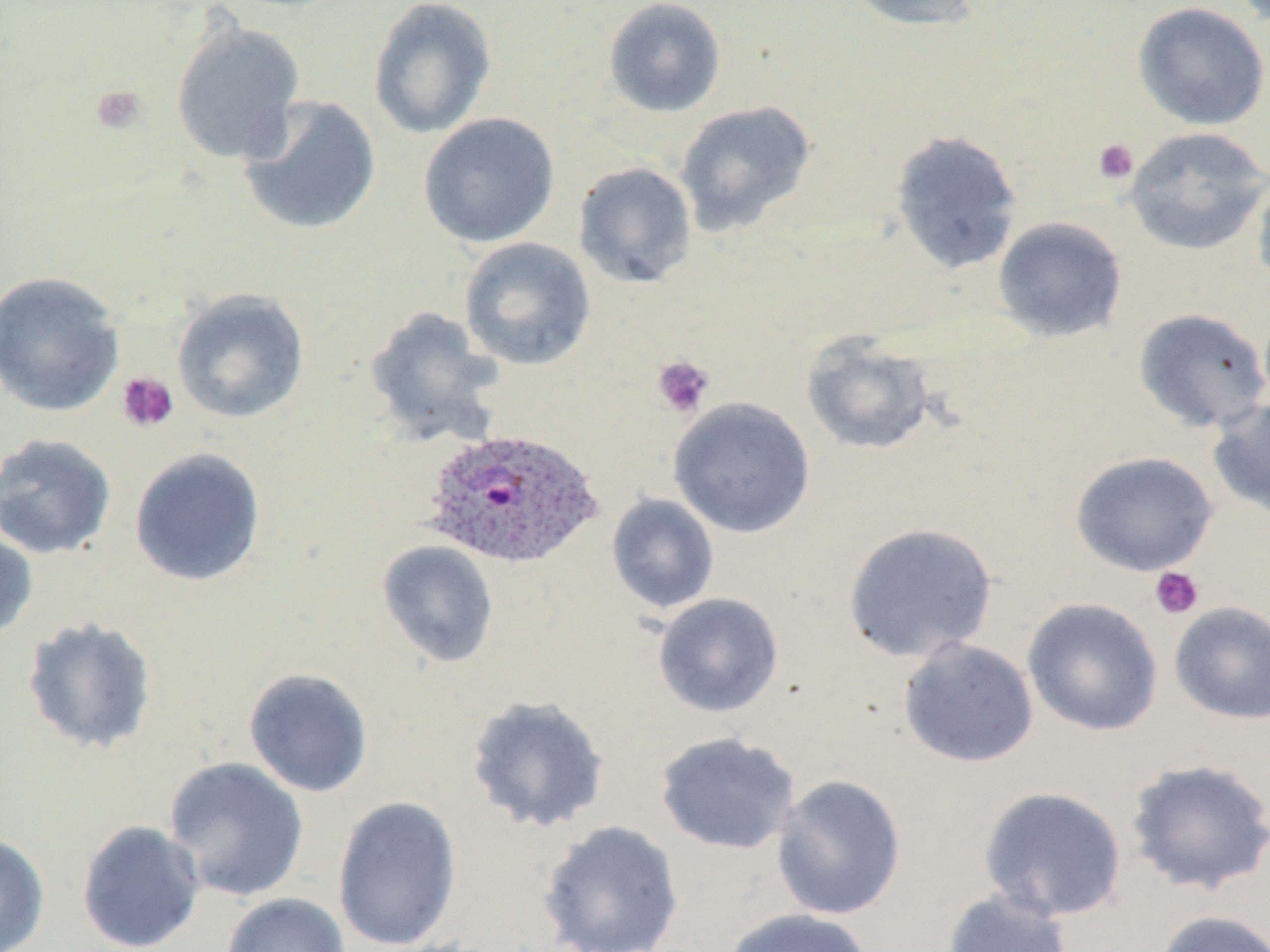
Summary:
  - Coordinate format: approximate bounding boxes as (x1, y1, x2, y2) in pixels
  - Uninfected red blood cell locations: (367, 0, 498, 140), (603, 0, 726, 118), (838, 0, 985, 33), (1131, 2, 1270, 131), (170, 18, 306, 165), (238, 95, 382, 237), (675, 100, 816, 237), (418, 112, 560, 248), (1124, 126, 1269, 255), (889, 129, 1023, 275), (573, 162, 697, 288), (1251, 171, 1270, 295), (993, 216, 1128, 343), (458, 236, 596, 371), (0, 271, 126, 417), (171, 288, 310, 424), (365, 306, 506, 449), (1133, 308, 1270, 434), (801, 331, 937, 456), (668, 397, 817, 538), (1207, 397, 1270, 521), (0, 433, 117, 560), (129, 447, 267, 587), (1070, 451, 1219, 577), (606, 493, 720, 614), (842, 522, 998, 663), (0, 524, 39, 645), (376, 540, 499, 668), (652, 592, 785, 718), (1022, 598, 1164, 737), (1168, 601, 1270, 724), (21, 616, 158, 755), (898, 638, 1039, 768), (243, 667, 374, 798), (465, 695, 610, 834), (655, 732, 801, 855), (162, 756, 310, 902), (1125, 758, 1270, 895), (771, 774, 907, 920), (978, 786, 1128, 922), (331, 796, 462, 952), (76, 819, 205, 952), (536, 819, 685, 952), (0, 832, 50, 952), (940, 888, 1074, 952), (220, 893, 350, 952), (721, 907, 874, 952), (1153, 909, 1270, 952)
  - Platelet locations: (89, 85, 148, 136), (1092, 139, 1139, 185), (652, 355, 714, 418), (116, 371, 179, 433), (1149, 566, 1204, 619)
  - Plasmodium ovale-infected red blood cell locations: (422, 427, 603, 570)
  - Slide-level diagnosis: Plasmodium ovale
  - Image size: 1270×952 pixels
  - Field of view: single
  - Magnification: 1000x
  - Stain: May-Grünwald-Giemsa
  - Preparation: thin blood film
  - Modality: optical microscopy